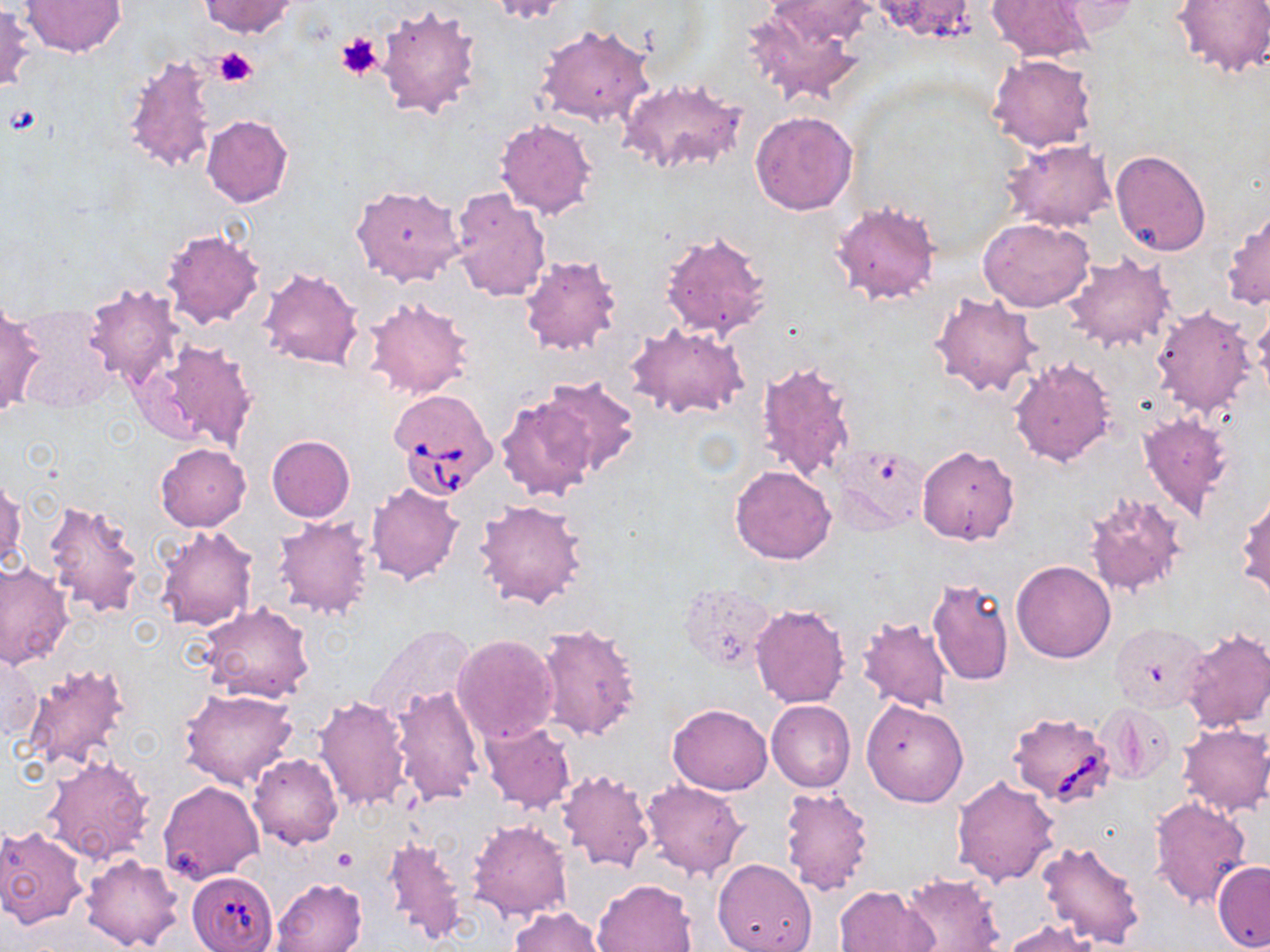

Approximate bounding boxes as named x1/y1/x2/y2 corners in pixels. Uninfected red blood cell locations: (x1=20, y1=0, x2=126, y2=56), (x1=199, y1=0, x2=298, y2=36), (x1=486, y1=0, x2=572, y2=23), (x1=765, y1=0, x2=877, y2=45), (x1=986, y1=0, x2=1093, y2=62), (x1=1171, y1=0, x2=1269, y2=78), (x1=1046, y1=1, x2=1141, y2=39), (x1=0, y1=3, x2=35, y2=94), (x1=374, y1=4, x2=483, y2=120), (x1=746, y1=6, x2=864, y2=105), (x1=535, y1=25, x2=654, y2=127), (x1=121, y1=54, x2=220, y2=173), (x1=988, y1=54, x2=1097, y2=153), (x1=618, y1=78, x2=749, y2=176), (x1=750, y1=110, x2=858, y2=216), (x1=202, y1=115, x2=293, y2=208), (x1=494, y1=117, x2=599, y2=220), (x1=1002, y1=140, x2=1116, y2=232), (x1=1109, y1=148, x2=1214, y2=257), (x1=351, y1=182, x2=465, y2=286), (x1=449, y1=186, x2=551, y2=304), (x1=829, y1=201, x2=940, y2=306), (x1=1222, y1=204, x2=1269, y2=310), (x1=978, y1=217, x2=1095, y2=313), (x1=161, y1=228, x2=266, y2=329), (x1=659, y1=230, x2=774, y2=340), (x1=1062, y1=252, x2=1178, y2=353), (x1=518, y1=254, x2=623, y2=357), (x1=258, y1=268, x2=364, y2=371), (x1=83, y1=282, x2=184, y2=390), (x1=930, y1=290, x2=1042, y2=397), (x1=365, y1=296, x2=475, y2=400), (x1=0, y1=302, x2=44, y2=418), (x1=1251, y1=305, x2=1270, y2=403), (x1=13, y1=306, x2=118, y2=411), (x1=1150, y1=306, x2=1256, y2=417), (x1=627, y1=324, x2=749, y2=420), (x1=144, y1=336, x2=259, y2=454), (x1=1009, y1=357, x2=1117, y2=466), (x1=754, y1=361, x2=858, y2=481), (x1=540, y1=373, x2=639, y2=475), (x1=495, y1=393, x2=600, y2=503), (x1=1136, y1=411, x2=1236, y2=521), (x1=266, y1=435, x2=356, y2=523), (x1=154, y1=443, x2=250, y2=531), (x1=917, y1=445, x2=1020, y2=545), (x1=834, y1=446, x2=929, y2=532), (x1=729, y1=465, x2=837, y2=565), (x1=1, y1=476, x2=25, y2=574), (x1=366, y1=482, x2=465, y2=586), (x1=1236, y1=490, x2=1270, y2=603), (x1=1084, y1=492, x2=1187, y2=598), (x1=41, y1=498, x2=145, y2=619), (x1=473, y1=498, x2=589, y2=610), (x1=271, y1=515, x2=376, y2=620), (x1=153, y1=525, x2=259, y2=632), (x1=1010, y1=560, x2=1116, y2=662), (x1=0, y1=561, x2=74, y2=671), (x1=926, y1=577, x2=1013, y2=687), (x1=678, y1=583, x2=775, y2=674), (x1=200, y1=602, x2=315, y2=703), (x1=750, y1=603, x2=851, y2=709), (x1=856, y1=618, x2=955, y2=712), (x1=535, y1=622, x2=642, y2=742), (x1=1110, y1=623, x2=1211, y2=713), (x1=366, y1=625, x2=477, y2=721), (x1=1181, y1=627, x2=1270, y2=733), (x1=451, y1=634, x2=558, y2=747), (x1=0, y1=651, x2=42, y2=743), (x1=21, y1=662, x2=131, y2=771), (x1=389, y1=684, x2=485, y2=805), (x1=181, y1=687, x2=298, y2=790), (x1=312, y1=696, x2=411, y2=811), (x1=766, y1=700, x2=855, y2=792), (x1=861, y1=700, x2=968, y2=806), (x1=668, y1=703, x2=773, y2=795), (x1=1099, y1=703, x2=1177, y2=784), (x1=479, y1=720, x2=577, y2=813), (x1=1177, y1=722, x2=1270, y2=817), (x1=42, y1=752, x2=154, y2=866), (x1=248, y1=753, x2=342, y2=849), (x1=556, y1=769, x2=656, y2=873), (x1=951, y1=775, x2=1060, y2=886), (x1=640, y1=779, x2=749, y2=881), (x1=158, y1=780, x2=265, y2=885), (x1=779, y1=786, x2=874, y2=894), (x1=1148, y1=796, x2=1251, y2=909), (x1=467, y1=818, x2=572, y2=921), (x1=0, y1=825, x2=90, y2=929), (x1=383, y1=836, x2=467, y2=945), (x1=1037, y1=840, x2=1145, y2=950), (x1=80, y1=853, x2=184, y2=950), (x1=713, y1=858, x2=817, y2=952), (x1=1212, y1=861, x2=1270, y2=951), (x1=896, y1=873, x2=1003, y2=952), (x1=270, y1=877, x2=366, y2=952), (x1=590, y1=879, x2=698, y2=952), (x1=833, y1=884, x2=936, y2=952), (x1=509, y1=906, x2=607, y2=952), (x1=1002, y1=919, x2=1099, y2=951). Babesia divergens-infected red blood cell locations: (x1=388, y1=388, x2=498, y2=496), (x1=1006, y1=712, x2=1117, y2=806), (x1=186, y1=870, x2=278, y2=952). Platelet locations: (x1=334, y1=32, x2=384, y2=79), (x1=212, y1=47, x2=257, y2=88), (x1=5, y1=102, x2=45, y2=138), (x1=333, y1=849, x2=357, y2=872). Slide-level diagnosis: Babesia divergens. Single field of view. Light microscopy. Image is 1270×952 pixels. May-Grünwald-Giemsa stain. 1000x magnification. Thin blood film.